Assess this cell for malaria.
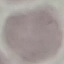
It is uninfected.

Acquired by smartphone through the microscope eyepiece. Automatically extracted cell patch, resized to 64 × 64 pixels. Giemsa stain. Thin smear of blood.